Identify the parasite.
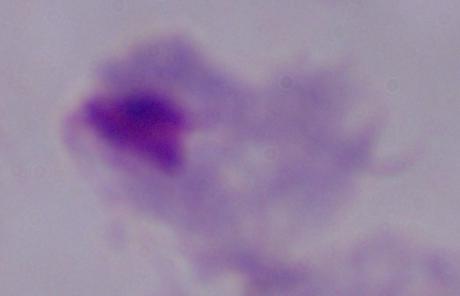

This is a trichomonad.

Summary:
  - Magnification: 1000x
  - Modality: micrograph